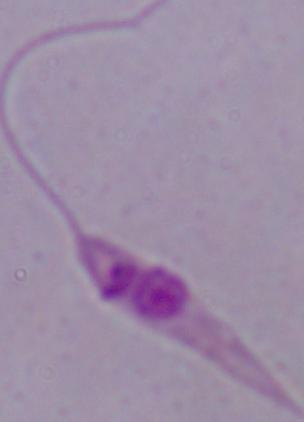
Summary:
  - Magnification: 1000x
  - Modality: micrograph
  - Identification: Leishmania